Assess this cell for malaria.
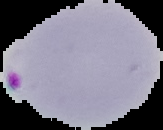
Parasitized.

Summary:
  - Preparation: thin blood film
  - Image type: cell region segmented out of the field of view; surrounding area masked to black
  - Image size: 163×130 pixels